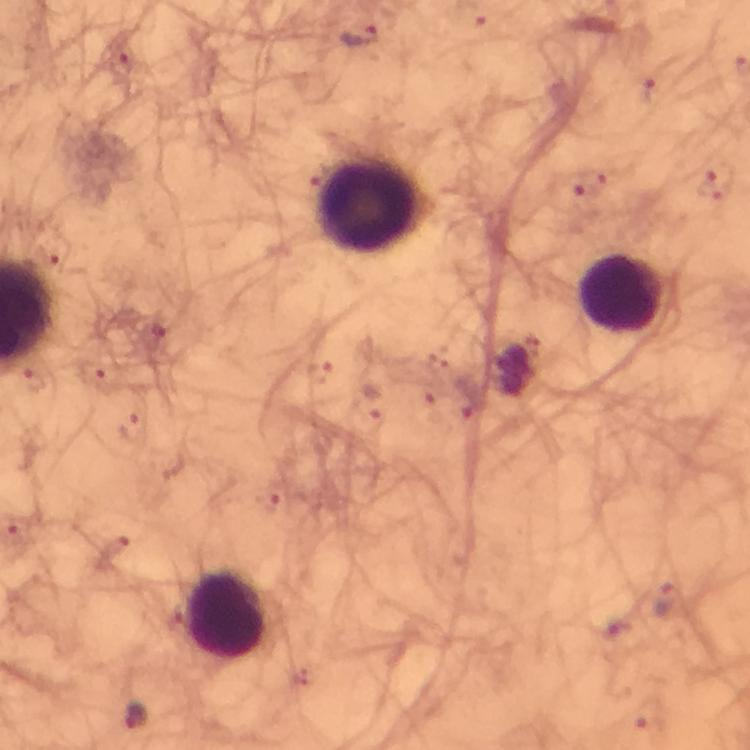
Approximate centers as [x, y] in pixels. Leukocyte locations: [370, 208], [621, 295], [226, 616]. Plasmodium parasite locations: [358, 37], [665, 599], [134, 717]. Giemsa stain. 100x magnification. Image is 750×750 pixels. Photographed through the microscope with a smartphone camera. Thick blood smear. Immersion oil applied. From a malaria diagnostic workup. Cropped region of a single field of view.